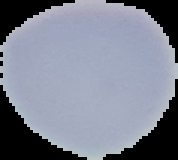

Image is 178×160 pixels. Result: no malaria parasites seen. The area outside the segmented cell region is set to black. From a thin blood film.